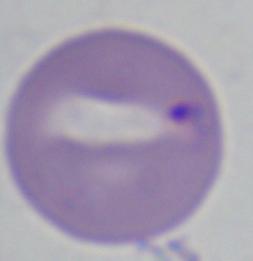

Summary:
  - Modality: photomicrograph
  - Magnification: 1000x
  - Identification: Babesia